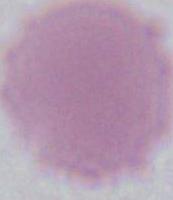
magnification = 1000x
identification = red blood cell
modality = micrograph